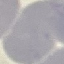
Malaria status: uninfected. Automatically extracted cell patch, resized to 64 × 64 pixels. Thin blood film. Giemsa-stained preparation. Acquired by smartphone through the microscope eyepiece.